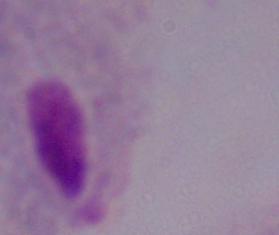
identification = trichomonad
modality = photomicrograph
magnification = 1000x